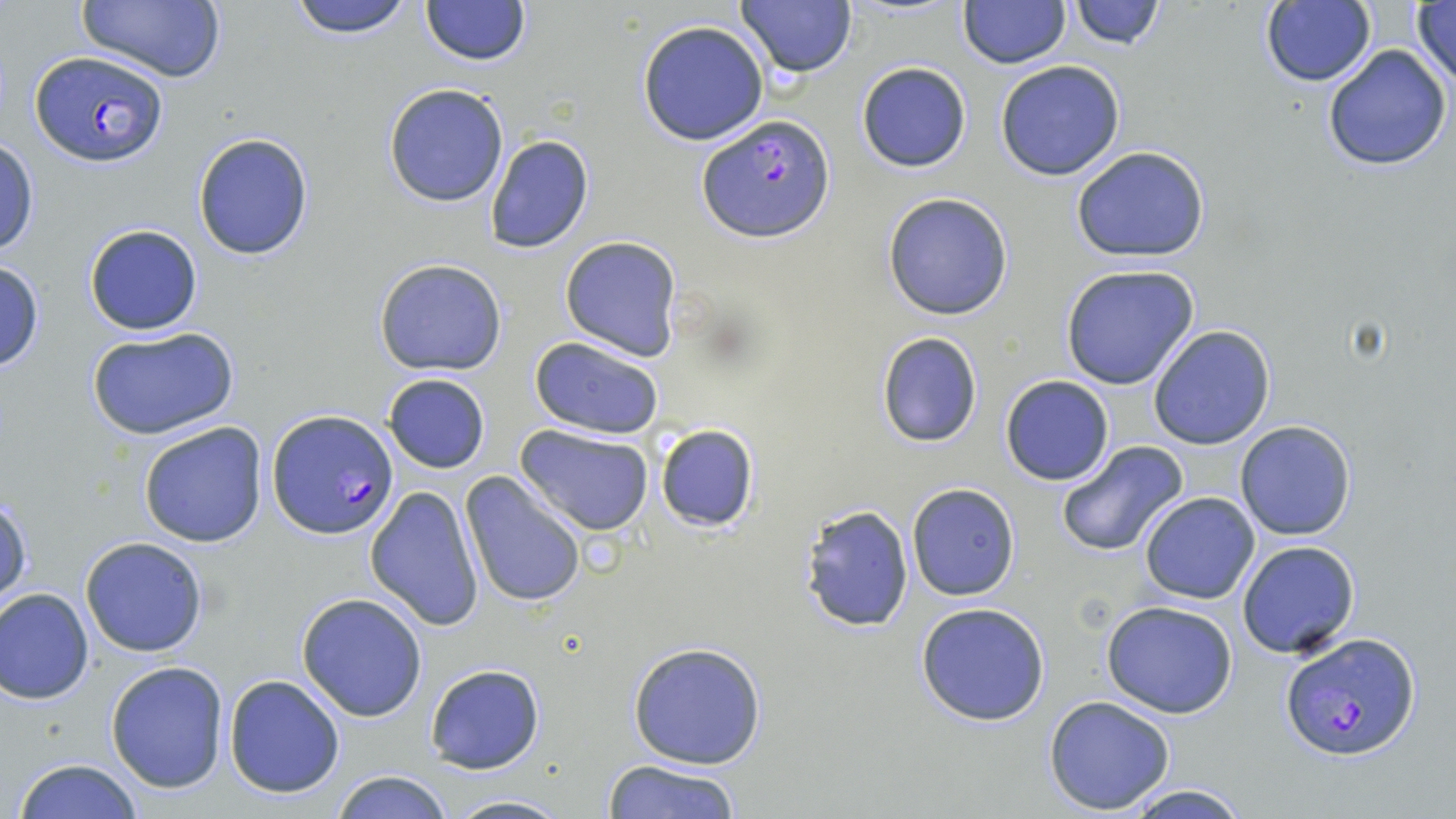
Approximate bounding boxes as (x1, y1, x2, y2) in pixels. Uninfected red blood cell locations: (287, 0, 416, 40), (421, 0, 532, 66), (735, 0, 857, 78), (1069, 0, 1165, 50), (75, 1, 229, 83), (958, 1, 1069, 69), (1258, 2, 1376, 87), (1411, 2, 1456, 91), (637, 20, 769, 146), (1321, 42, 1453, 172), (994, 59, 1126, 181), (855, 61, 972, 173), (383, 83, 509, 208), (192, 131, 315, 263), (483, 134, 594, 255), (0, 135, 39, 258), (1071, 145, 1210, 262), (882, 191, 1014, 320), (82, 223, 204, 336), (558, 236, 683, 360), (0, 258, 44, 374), (373, 258, 507, 376), (1059, 264, 1204, 391), (86, 326, 239, 440), (1147, 326, 1276, 448), (875, 331, 984, 449), (530, 336, 665, 440), (382, 372, 491, 474), (999, 375, 1114, 486), (138, 420, 268, 548), (1234, 421, 1357, 541), (515, 424, 654, 537), (654, 424, 760, 533), (1055, 441, 1189, 558), (459, 472, 586, 608), (906, 483, 1020, 601), (365, 485, 484, 630), (1139, 493, 1259, 605), (801, 504, 916, 635), (80, 535, 210, 657), (1237, 540, 1360, 659), (0, 586, 94, 704), (296, 592, 428, 722), (1101, 601, 1239, 719), (916, 602, 1050, 727), (627, 640, 769, 770), (106, 661, 230, 794), (423, 664, 546, 774), (223, 674, 345, 798), (1044, 695, 1176, 815), (604, 757, 741, 819), (12, 759, 146, 818), (329, 768, 455, 819), (1119, 783, 1254, 818), (438, 793, 574, 818). Plasmodium falciparum-infected red blood cell locations: (29, 52, 168, 166), (698, 115, 837, 243), (267, 409, 400, 540), (1280, 631, 1421, 761). Slide-level diagnosis: Plasmodium falciparum. May-Grünwald-Giemsa stain. Thin blood smear. Single field of view. 1000x magnification. Optical microscopy. Image is 1456×819 pixels.